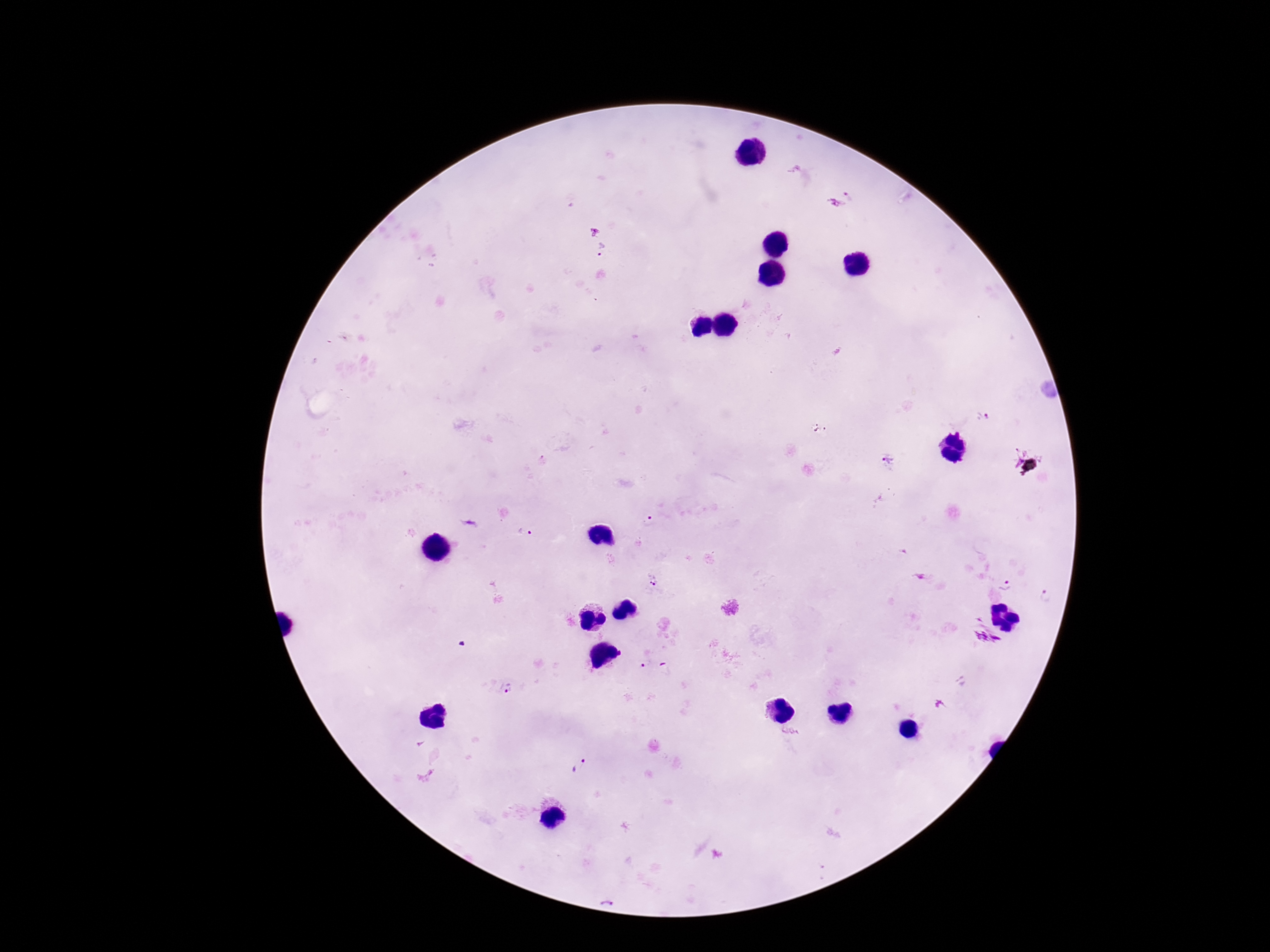

Approximate object centers, in pixels from the top-left corner. Plasmodium parasite locations: (x=849, y=195), (x=835, y=204), (x=602, y=249), (x=983, y=416), (x=888, y=457), (x=649, y=518), (x=524, y=532), (x=654, y=581), (x=1007, y=585), (x=1046, y=594), (x=643, y=666), (x=507, y=689), (x=580, y=766). Image is 1270×952 pixels. 100x magnification. Smartphone photograph taken through the microscope eyepiece. Patient malaria status: infected. One field from this slide. Thick blood smear. Giemsa stain.